Give the preparation type.
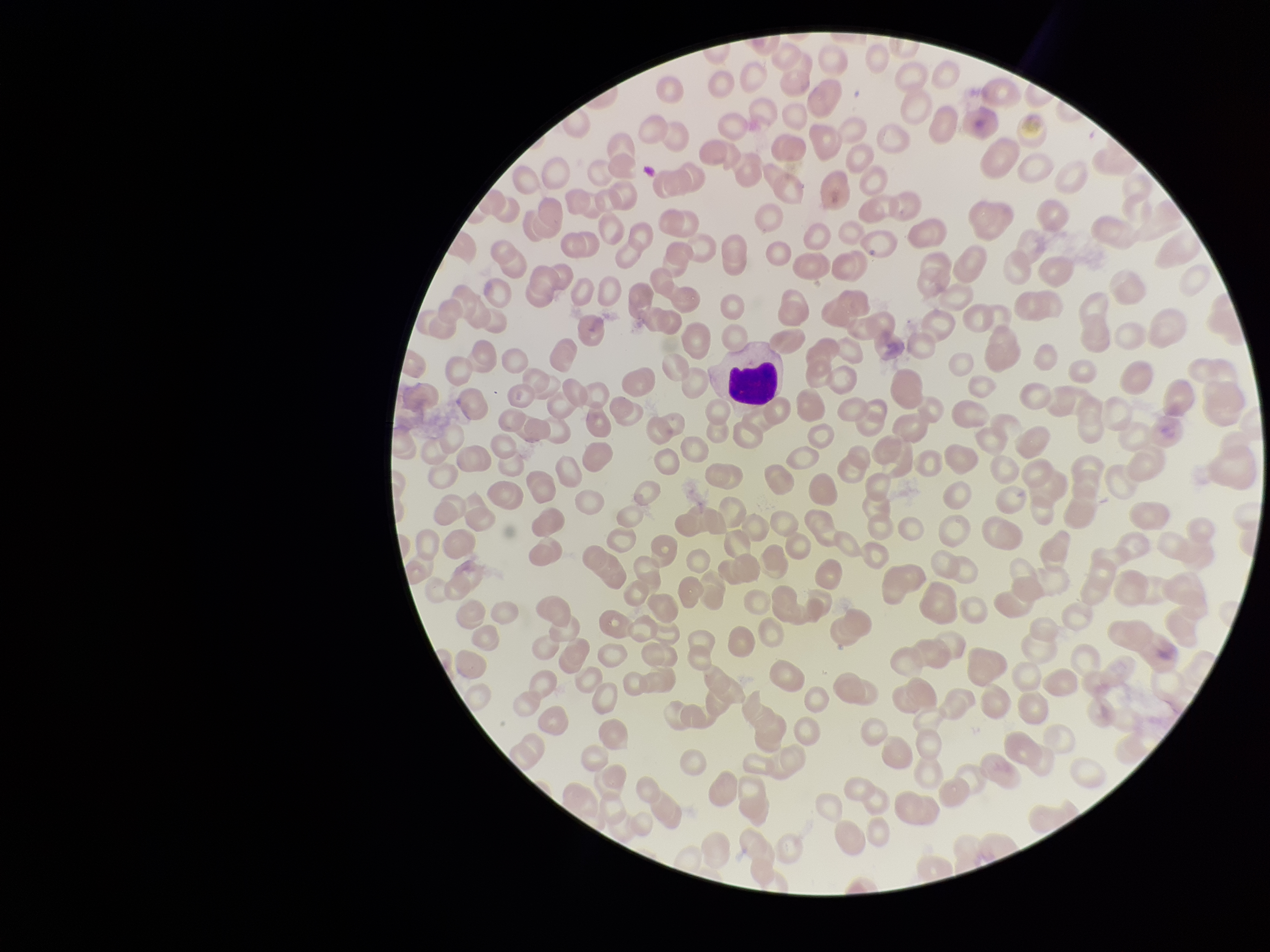

It is a thin blood smear.

Parasitized red blood cells: none seen. Patient malaria status: negative. Parasitized red blood cell count: 0. Red blood cell count: 247. Image is 1270×952 pixels. Single field of view. Giemsa stain. Photographed through the microscope eyepiece with a smartphone camera.